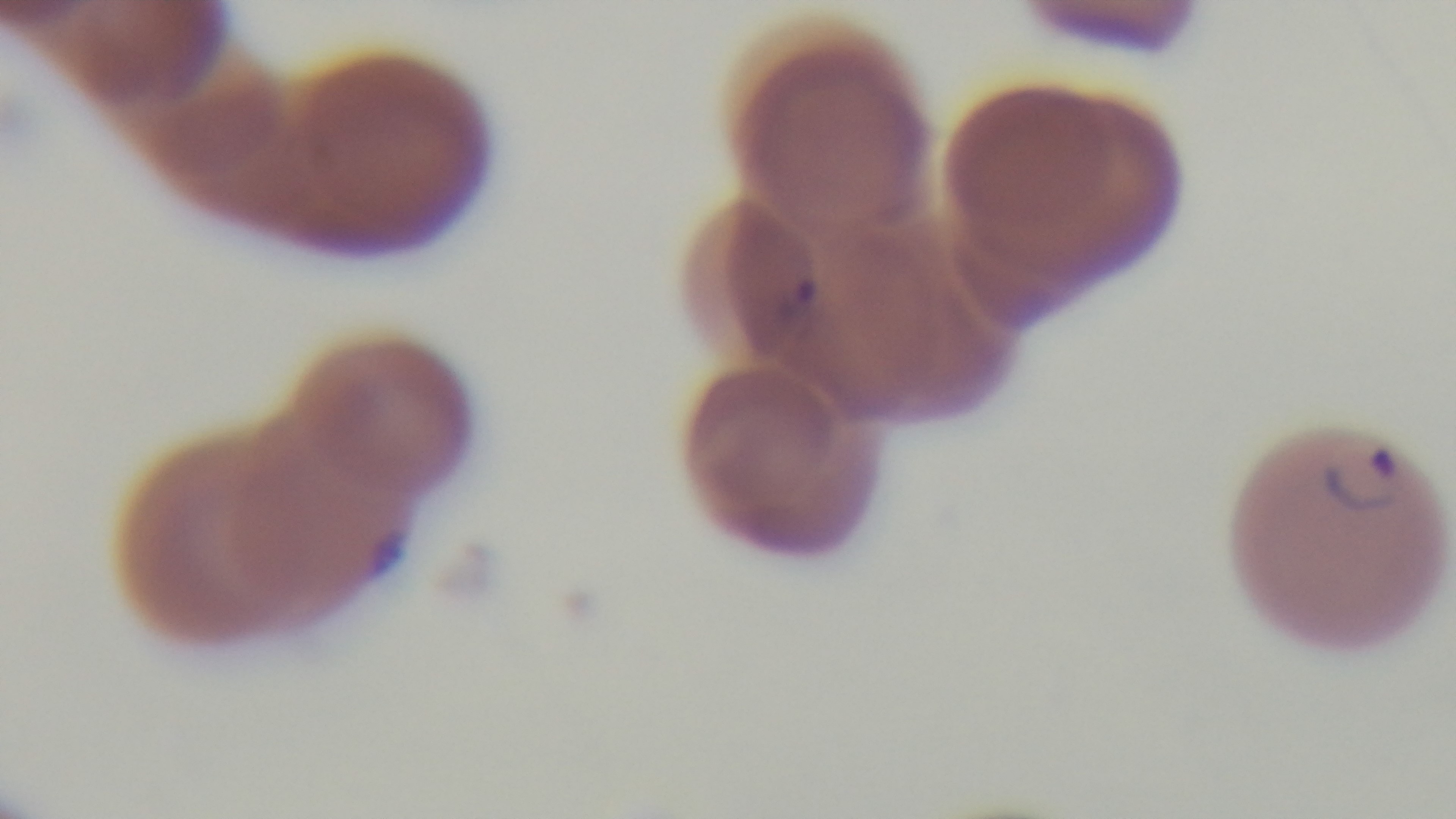 One field from the slide. Photomicrograph. 100x oil-immersion objective. Mounted 4K digital camera. Malaria status: infected. Preparation: thin blood film. Giemsa-stained.